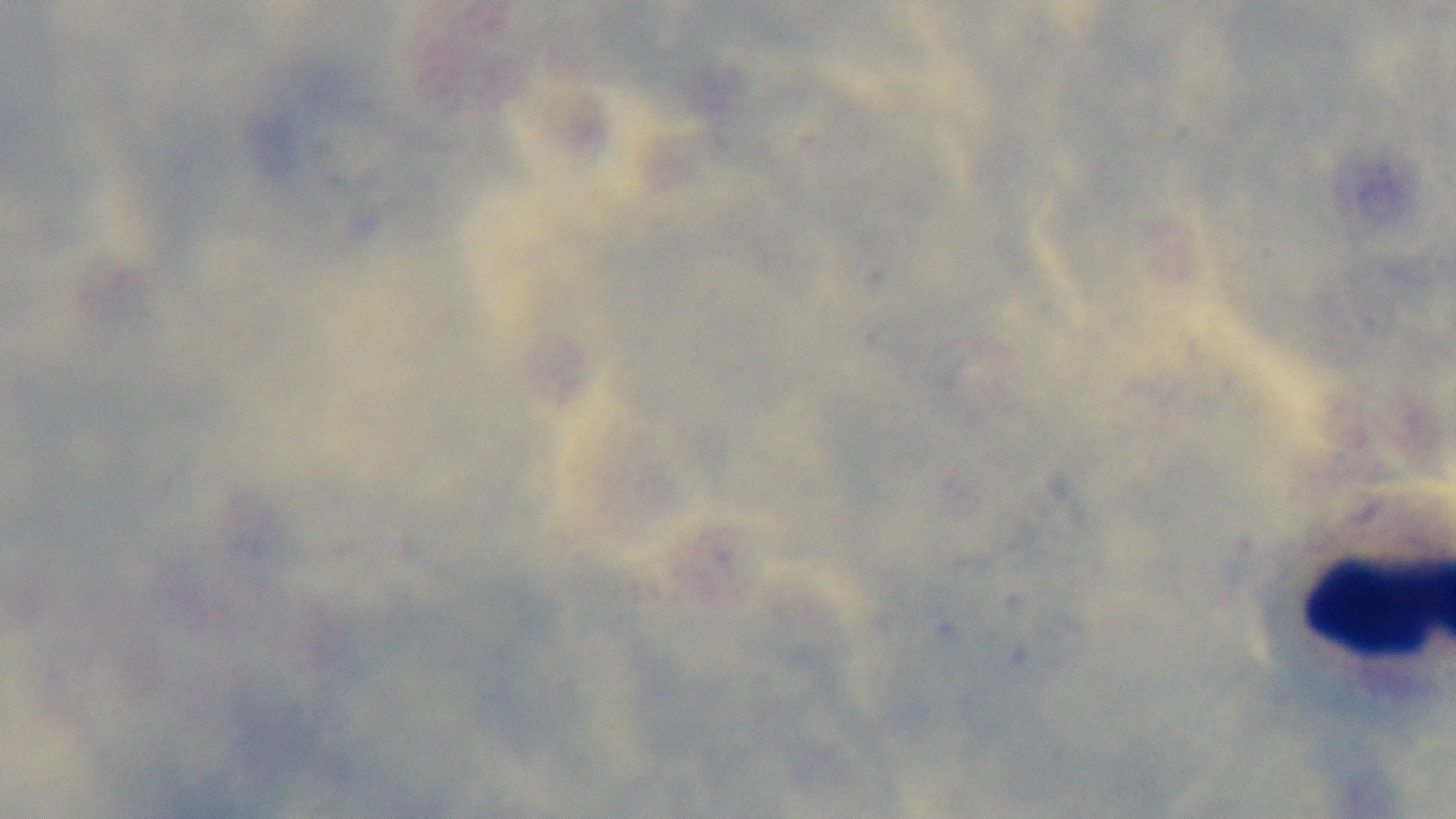

malaria status = uninfected
field of view = single
capture = mounted 4K digital camera
preparation = thick
objective = 100x oil immersion
stain = Giemsa
modality = light microscopy